Report the malaria status of this cell.
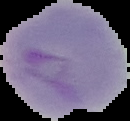

It is parasitized.

preparation: thin blood film
image_type: segmented cell region on a black background
image_size: 130×121 pixels